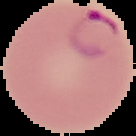

Summary:
  - Preparation: thin blood film
  - Malaria status: parasitized
  - Image type: segmented cell region on a black background
  - Image size: 136×136 pixels